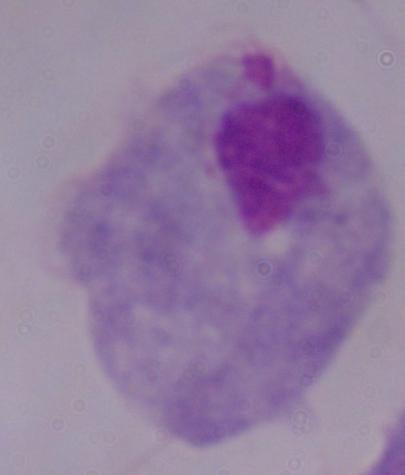

{
  "modality": "photomicrograph",
  "magnification": "1000x",
  "identification": "trichomonad"
}